Outline each uninfected red blood cell.
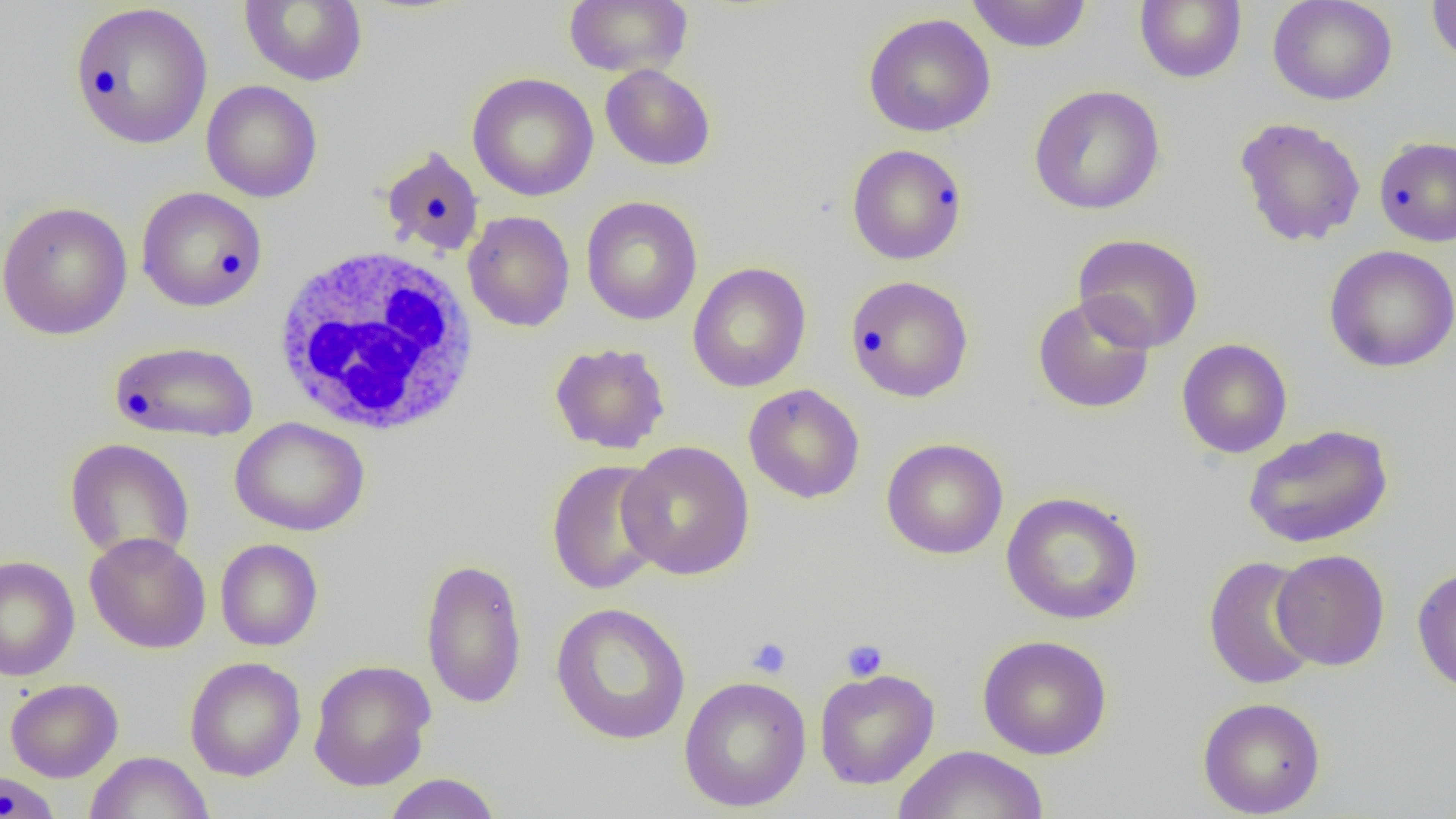
Approximate bounding boxes as (x1, y1, x2, y2) in pixels.
Uninfected red blood cells: (239, 0, 368, 87), (564, 0, 692, 77), (966, 0, 1092, 53), (1135, 0, 1246, 84), (1268, 0, 1398, 105), (1426, 0, 1456, 68), (69, 3, 213, 149), (863, 12, 996, 138), (600, 64, 716, 171), (467, 72, 598, 202), (201, 80, 323, 203), (1028, 85, 1165, 214), (1234, 117, 1367, 247), (1373, 135, 1456, 247), (847, 144, 967, 265), (380, 146, 485, 257), (136, 186, 267, 312), (581, 196, 702, 325), (0, 200, 133, 341), (462, 210, 575, 332), (1072, 233, 1204, 353), (1324, 245, 1456, 373), (687, 262, 812, 393), (845, 275, 974, 402), (1032, 294, 1155, 414), (1177, 338, 1292, 459), (109, 340, 259, 442), (549, 342, 671, 455), (743, 384, 865, 504), (230, 416, 370, 537), (1242, 424, 1394, 549), (881, 437, 1008, 559), (65, 438, 195, 563), (617, 440, 756, 581), (546, 459, 668, 595), (1001, 491, 1144, 625), (84, 532, 212, 653), (215, 539, 323, 651), (1271, 549, 1389, 670), (0, 554, 80, 681), (1204, 556, 1321, 690), (419, 557, 528, 709), (1411, 564, 1455, 697), (550, 602, 691, 745), (977, 634, 1112, 760), (185, 657, 306, 781), (308, 659, 436, 791), (815, 668, 939, 789), (678, 675, 812, 812), (5, 678, 123, 782), (1197, 696, 1326, 817), (893, 745, 1049, 819), (84, 751, 214, 818), (1, 769, 61, 818), (381, 773, 502, 819).

Summary:
  - White blood cell locations: (271, 245, 482, 437)
  - Platelet locations: (746, 637, 792, 679), (841, 639, 888, 682)
  - Slide-level diagnosis: negative for blood parasites
  - Field of view: single
  - Magnification: 1000x
  - Modality: optical microscopy
  - Image size: 1456×819 pixels
  - Preparation: thin blood smear